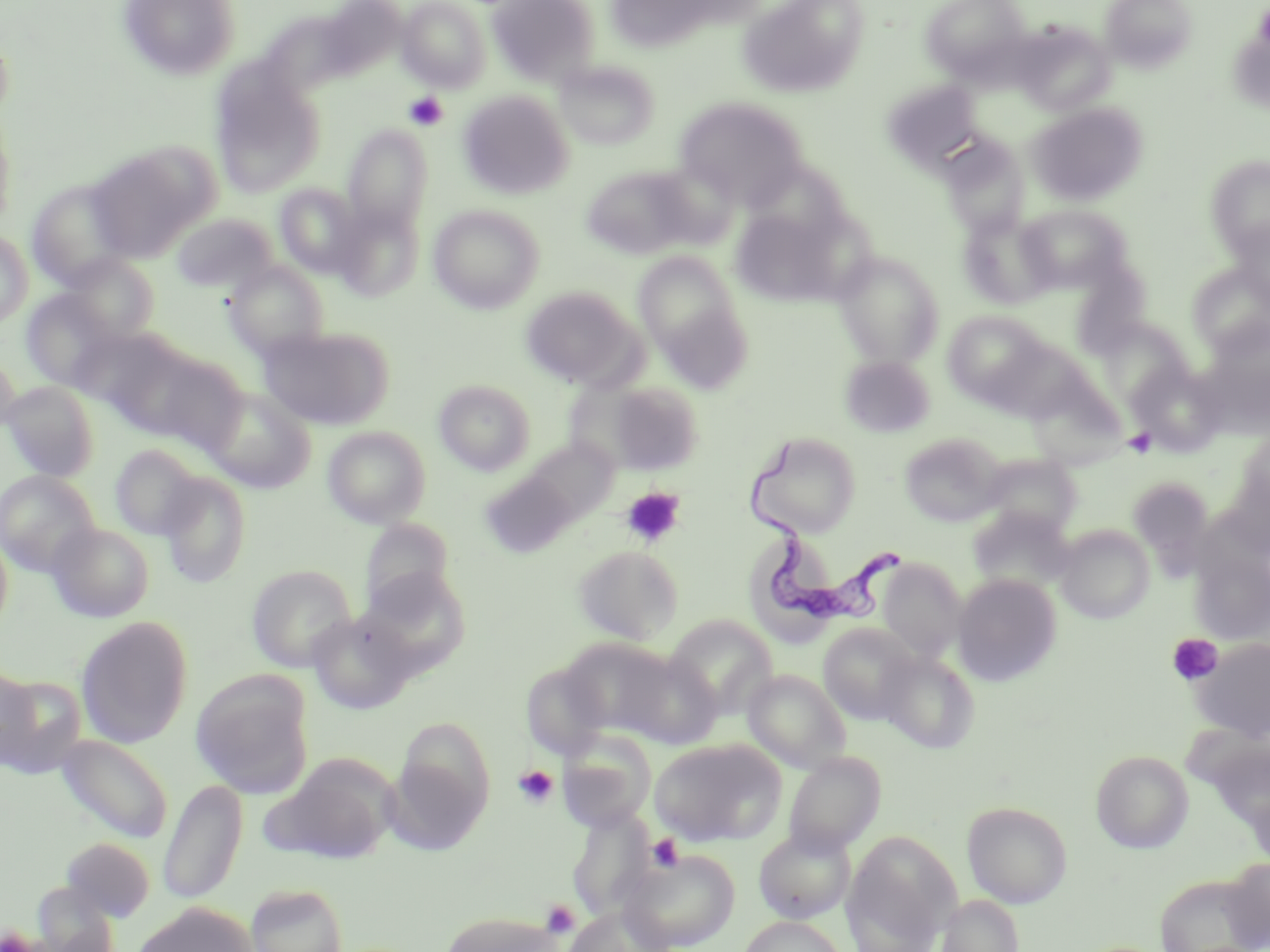
Summary:
  - Coordinate format: approximate bounding boxes as [x1, y1, x2, y2] in pixels
  - Platelet locations: [404, 92, 449, 131], [1123, 428, 1157, 458], [620, 487, 685, 548], [1167, 633, 1223, 686], [513, 764, 558, 807], [647, 833, 684, 872], [541, 900, 579, 938]
  - Trypanosoma brucei locations: [752, 439, 907, 634]
  - Uninfected red blood cell locations: [118, 0, 241, 81], [487, 0, 599, 85], [738, 0, 869, 98], [920, 0, 1033, 83], [1103, 0, 1196, 73], [397, 1, 491, 91], [610, 3, 712, 57], [1015, 23, 1115, 115], [0, 27, 15, 123], [554, 59, 660, 150], [210, 65, 325, 198], [883, 79, 984, 170], [458, 91, 574, 200], [673, 96, 809, 209], [1028, 103, 1147, 206], [0, 110, 16, 233], [342, 125, 433, 230], [940, 134, 1031, 237], [87, 145, 213, 263], [1206, 156, 1270, 258], [745, 160, 852, 247], [646, 162, 742, 250], [580, 164, 699, 261], [26, 179, 136, 289], [275, 184, 366, 277], [332, 203, 425, 301], [428, 204, 545, 314], [1016, 204, 1130, 294], [730, 207, 843, 305], [959, 211, 1058, 310], [173, 213, 279, 294], [1229, 218, 1270, 311], [0, 230, 33, 329], [632, 250, 746, 365], [832, 250, 945, 368], [64, 255, 159, 342], [224, 260, 329, 359], [1186, 263, 1270, 356], [520, 286, 640, 387], [21, 289, 119, 390], [942, 310, 1050, 408], [1202, 320, 1270, 426], [261, 326, 392, 430], [0, 352, 20, 436], [143, 352, 250, 454], [840, 356, 934, 437], [1128, 363, 1224, 455], [434, 379, 536, 476], [1025, 379, 1127, 469], [598, 380, 705, 476], [2, 381, 100, 482], [203, 387, 315, 493], [322, 426, 431, 528], [745, 431, 862, 538], [1236, 431, 1270, 518], [899, 432, 1006, 527], [518, 437, 620, 529], [110, 445, 203, 540], [981, 454, 1083, 538], [1221, 468, 1270, 560], [0, 469, 101, 576], [482, 469, 580, 558], [159, 472, 252, 588], [359, 519, 454, 616], [47, 522, 155, 622], [1055, 524, 1155, 624], [0, 533, 14, 633], [573, 545, 683, 644], [1190, 546, 1269, 645], [878, 560, 966, 660], [247, 564, 356, 672], [360, 568, 471, 673], [952, 574, 1061, 687], [308, 610, 416, 713], [664, 614, 778, 718], [76, 616, 194, 748], [818, 623, 919, 724], [1191, 637, 1270, 742], [619, 650, 722, 749], [879, 651, 981, 753], [521, 661, 612, 760], [0, 667, 37, 773], [742, 670, 851, 772], [191, 671, 314, 799], [0, 674, 88, 777], [391, 714, 496, 841], [556, 728, 657, 831], [55, 734, 173, 844], [649, 738, 787, 846], [1091, 750, 1193, 853], [784, 752, 884, 855], [262, 758, 398, 864], [158, 779, 248, 905], [962, 801, 1072, 908], [567, 810, 657, 919], [753, 826, 856, 924], [841, 831, 961, 951], [61, 837, 156, 922], [622, 848, 741, 950], [1221, 856, 1270, 951], [1156, 873, 1263, 951], [32, 880, 123, 952], [245, 882, 349, 952], [937, 894, 1023, 952], [134, 903, 258, 952], [562, 904, 672, 952], [438, 911, 568, 952], [738, 915, 848, 952]
  - Slide-level diagnosis: Trypanosoma brucei
  - Preparation: thin blood film
  - Magnification: 1000x
  - Modality: optical microscopy
  - Stain: May-Grünwald-Giemsa
  - Image size: 1270×952 pixels
  - Field of view: single